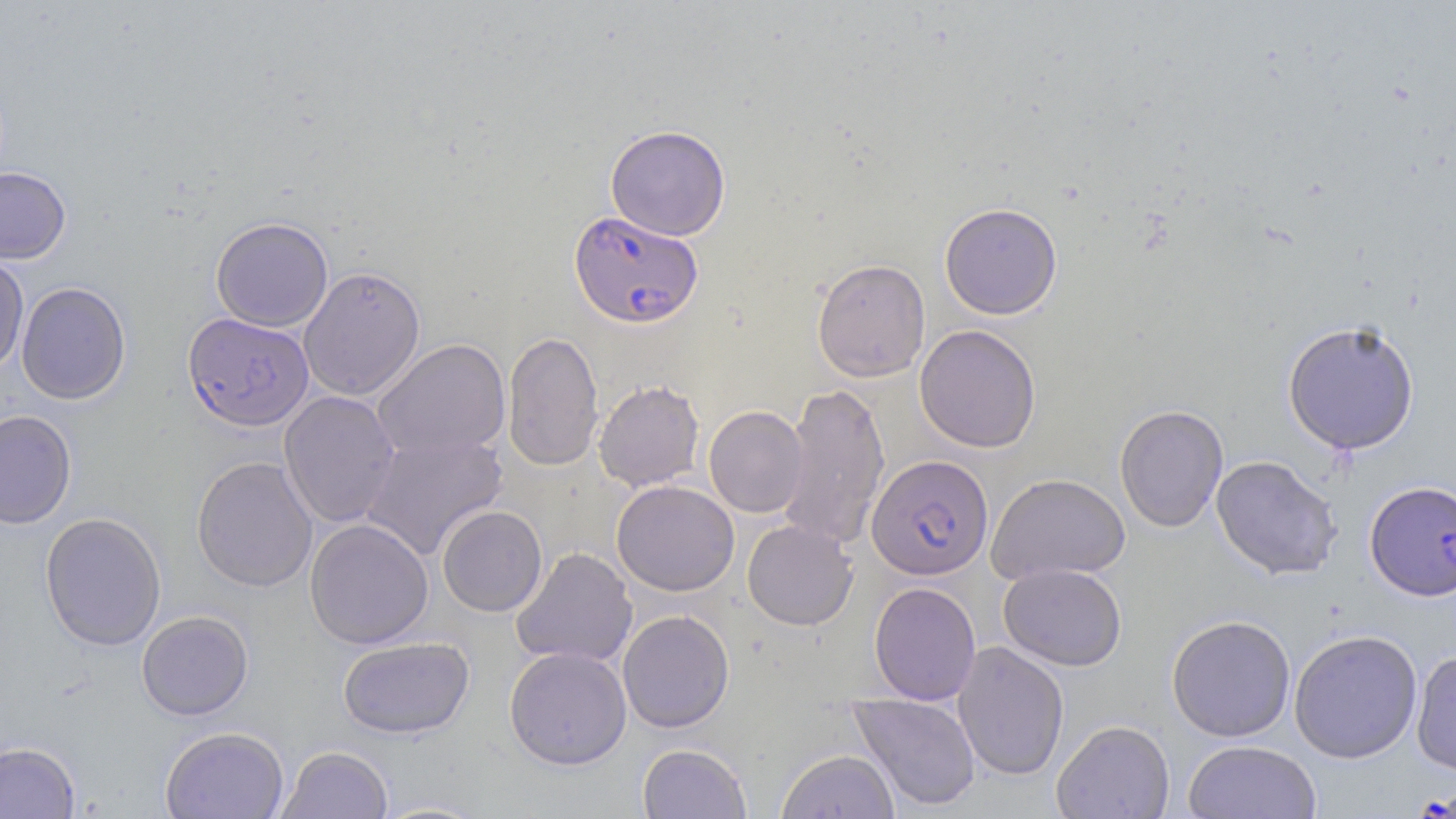

slide-level diagnosis = Plasmodium falciparum
image size = 1456×819 pixels
modality = light microscopy
preparation = thin blood smear
stain = May-Grünwald-Giemsa
Plasmodium falciparum-infected red blood cell locations = approximate bounding boxes as [x1, y1, x2, y2] in pixels: [569, 210, 703, 328], [182, 312, 313, 432], [867, 454, 993, 579], [1365, 480, 1456, 600]
uninfected red blood cell locations = approximate bounding boxes as [x1, y1, x2, y2] in pixels: [605, 124, 730, 241], [0, 167, 71, 264], [939, 202, 1062, 320], [210, 217, 333, 332], [0, 253, 29, 375], [812, 258, 930, 382], [298, 266, 425, 401], [16, 282, 131, 405], [1282, 319, 1420, 455], [915, 324, 1041, 452], [502, 331, 604, 472], [373, 339, 511, 462], [593, 379, 704, 491], [778, 381, 890, 552], [279, 391, 400, 528], [1114, 404, 1228, 532], [704, 405, 808, 518], [0, 410, 77, 529], [360, 431, 507, 561], [1211, 454, 1343, 580], [192, 455, 318, 592], [987, 473, 1130, 584], [611, 480, 739, 596], [437, 505, 547, 616], [40, 511, 167, 651], [304, 518, 433, 649], [742, 520, 858, 630], [511, 547, 638, 668], [999, 563, 1127, 671], [868, 581, 981, 705], [618, 609, 735, 733], [136, 610, 253, 720], [1166, 614, 1296, 742], [1288, 628, 1423, 763], [337, 636, 474, 739], [952, 641, 1069, 781], [504, 646, 631, 769], [1411, 648, 1456, 776], [849, 692, 981, 812], [1051, 719, 1174, 818], [160, 726, 289, 819], [1183, 740, 1322, 819], [0, 741, 81, 818], [637, 743, 752, 818], [277, 745, 393, 819], [776, 748, 900, 819], [372, 799, 491, 818]
magnification = 1000x
field of view = one of a larger specimen